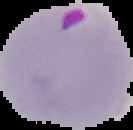
Summary:
  - Image size: 133×130 pixels
  - Image type: segmented cell region with the area outside set to black
  - Preparation: thin blood smear
  - Result: malaria parasites detected